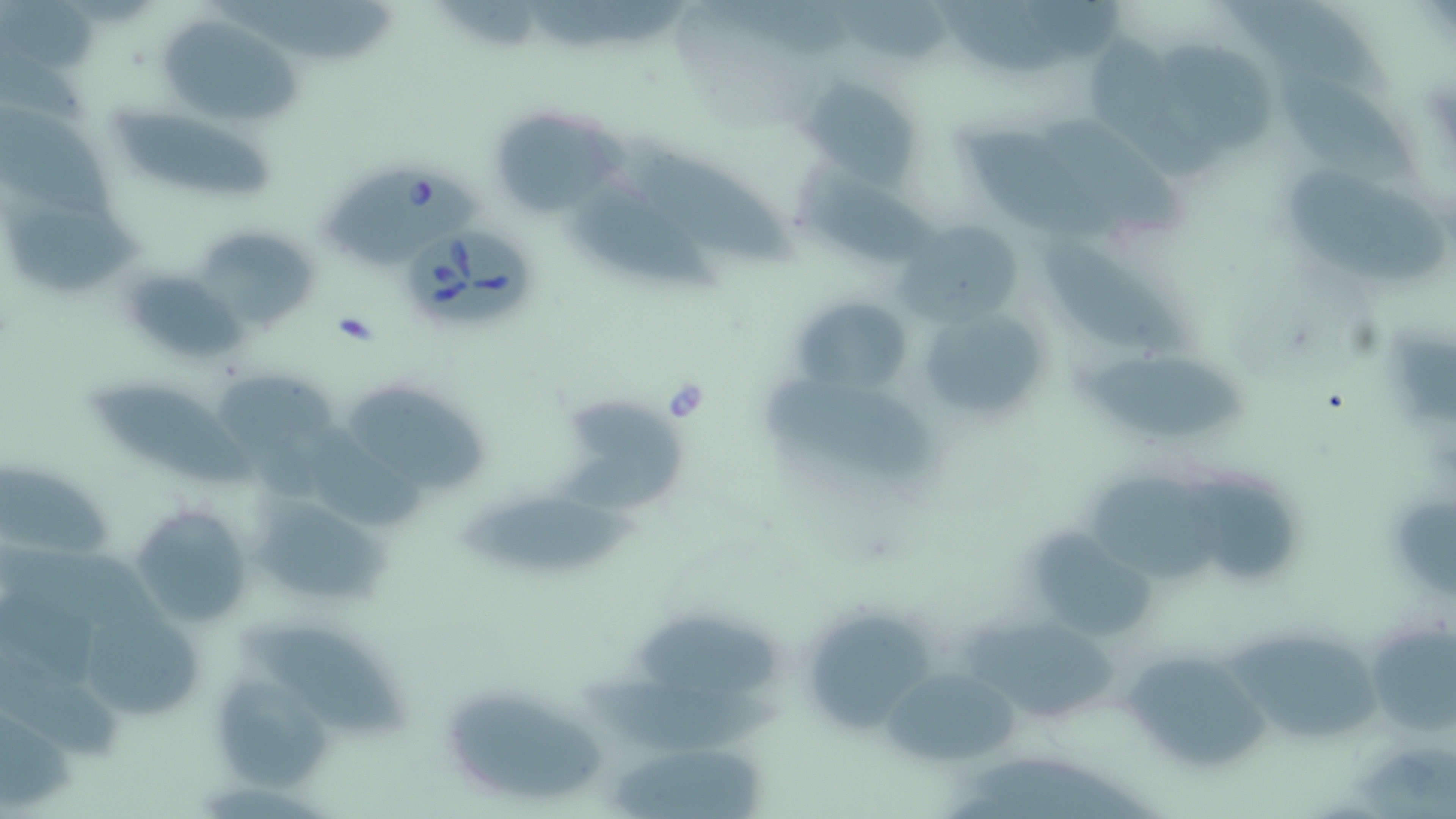
slide-level diagnosis = Babesia divergens
modality = light microscopy
stain = May-Grünwald-Giemsa
Babesia divergens-infected red blood cell locations = approximate bounding boxes as [x1, y1, x2, y2] in pixels: [316, 165, 481, 267], [406, 230, 538, 329]
field of view = single
magnification = 1000x
uninfected red blood cell locations = approximate bounding boxes as [x1, y1, x2, y2] in pixels: [209, 0, 398, 63], [1223, 1, 1394, 105], [157, 13, 301, 128], [1079, 32, 1224, 182], [1160, 43, 1284, 155], [1275, 72, 1421, 182], [803, 77, 918, 183], [1, 104, 121, 220], [105, 104, 276, 202], [487, 106, 625, 217], [1044, 118, 1192, 237], [961, 127, 1111, 237], [603, 135, 796, 264], [796, 167, 941, 261], [1292, 170, 1447, 286], [566, 181, 719, 294], [5, 200, 151, 294], [897, 216, 1029, 327], [196, 232, 319, 331], [1038, 242, 1196, 361], [131, 271, 248, 357], [791, 295, 912, 398], [913, 301, 1051, 427], [1079, 354, 1255, 437], [202, 360, 346, 456], [751, 374, 942, 484], [90, 378, 261, 487], [342, 383, 489, 493], [556, 393, 692, 517], [306, 426, 428, 530], [0, 459, 117, 564], [1089, 476, 1228, 587], [1184, 480, 1304, 582], [245, 488, 393, 612], [456, 492, 639, 578], [129, 503, 256, 630], [1035, 524, 1158, 639], [630, 611, 788, 698], [807, 617, 936, 732], [1365, 617, 1453, 738], [961, 618, 1127, 723], [87, 621, 212, 720], [243, 623, 416, 735], [1220, 630, 1388, 741], [0, 646, 125, 764], [1118, 658, 1274, 774], [879, 664, 1024, 765], [568, 671, 788, 756], [216, 680, 338, 794], [441, 683, 604, 805], [601, 745, 774, 819]
preparation = thin blood smear
image size = 1456×819 pixels